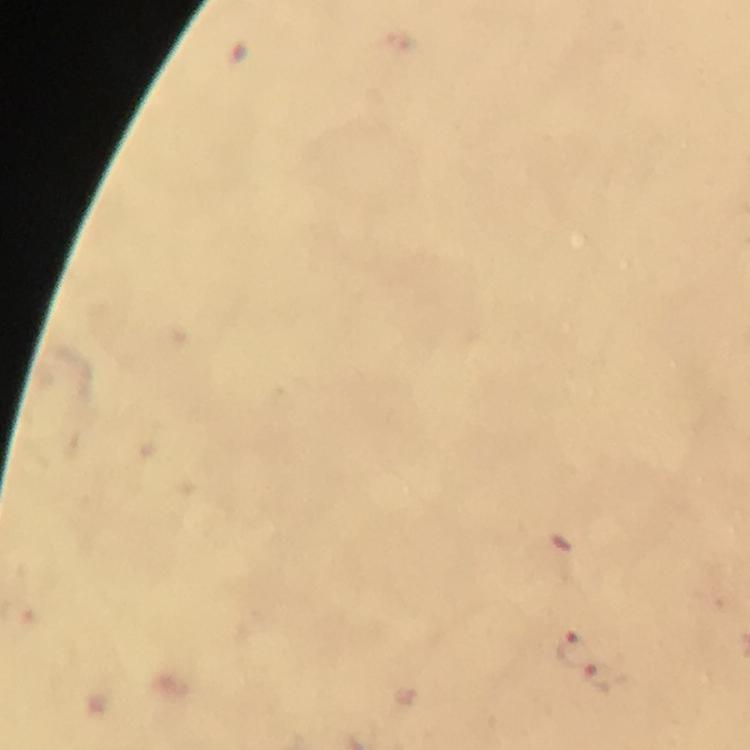

Approximate centers as (x, y) in pixels.
Summary:
  - Malaria parasite locations: (569, 648), (602, 676)
  - Immersion oil: used
  - Preparation: thick blood smear
  - Capture: smartphone mounted on the microscope
  - Cropped from: one field of view
  - Context: from a malaria diagnostic workup
  - Stain: Giemsa
  - Magnification: 100x
  - Image size: 750×750 pixels